Outline each Plasmodium falciparum-infected red blood cell.
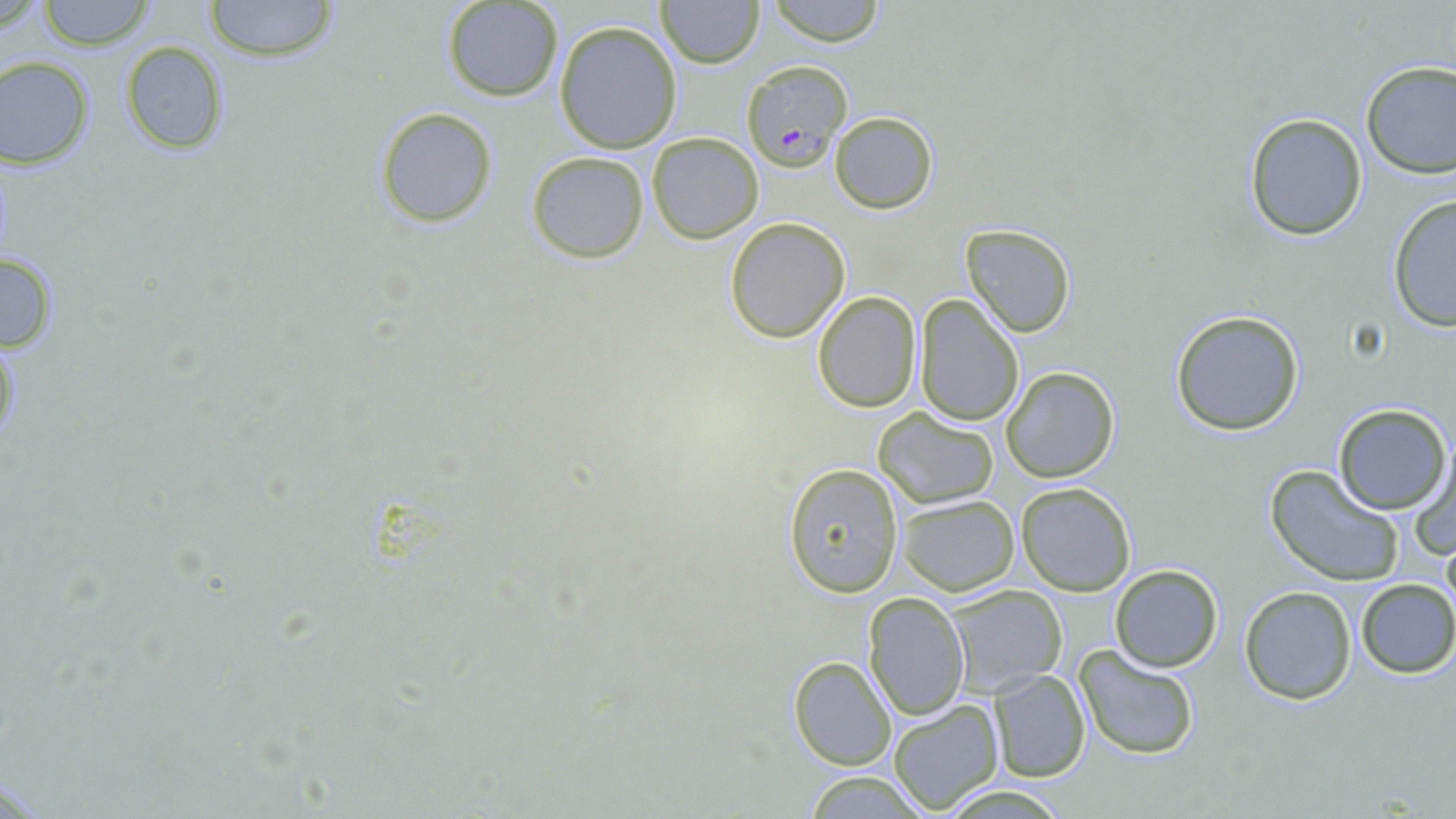

Approximate bounding boxes as named x1/y1/x2/y2 corners in pixels.
Plasmodium falciparum-infected red blood cells: (x1=739, y1=59, x2=852, y2=171).

{
  "slide_level_diagnosis": "Plasmodium falciparum",
  "stain": "May-Grünwald-Giemsa",
  "field_of_view": "single",
  "image_size": "1456×819 pixels",
  "uninfected_red_blood_cell_locations": "approximate bounding boxes as named x1/y1/x2/y2 corners in pixels: (x1=201, y1=0, x2=341, y2=64), (x1=440, y1=0, x2=565, y2=102), (x1=656, y1=0, x2=764, y2=68), (x1=765, y1=0, x2=888, y2=46), (x1=35, y1=1, x2=157, y2=50), (x1=553, y1=20, x2=682, y2=154), (x1=118, y1=41, x2=231, y2=155), (x1=0, y1=58, x2=95, y2=170), (x1=1358, y1=59, x2=1456, y2=179), (x1=374, y1=107, x2=498, y2=229), (x1=828, y1=109, x2=939, y2=215), (x1=1242, y1=113, x2=1368, y2=241), (x1=644, y1=131, x2=764, y2=243), (x1=525, y1=151, x2=649, y2=262), (x1=1385, y1=194, x2=1456, y2=331), (x1=724, y1=218, x2=850, y2=342), (x1=959, y1=223, x2=1077, y2=338), (x1=0, y1=251, x2=59, y2=355), (x1=812, y1=290, x2=921, y2=412), (x1=915, y1=294, x2=1026, y2=427), (x1=1169, y1=310, x2=1306, y2=436), (x1=1001, y1=366, x2=1120, y2=482), (x1=1331, y1=402, x2=1452, y2=515), (x1=873, y1=407, x2=999, y2=508), (x1=1407, y1=445, x2=1456, y2=561), (x1=782, y1=463, x2=904, y2=597), (x1=1266, y1=466, x2=1404, y2=589), (x1=1016, y1=482, x2=1136, y2=596), (x1=896, y1=494, x2=1020, y2=596), (x1=1442, y1=530, x2=1456, y2=618), (x1=1109, y1=565, x2=1223, y2=673), (x1=1354, y1=578, x2=1456, y2=677), (x1=944, y1=584, x2=1067, y2=697), (x1=1239, y1=586, x2=1358, y2=705), (x1=862, y1=590, x2=970, y2=719), (x1=1075, y1=646, x2=1202, y2=763), (x1=788, y1=655, x2=897, y2=771), (x1=986, y1=669, x2=1091, y2=783), (x1=888, y1=701, x2=1004, y2=813), (x1=796, y1=771, x2=929, y2=817)",
  "magnification": "1000x",
  "preparation": "thin blood smear",
  "modality": "light microscopy"
}